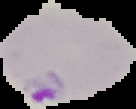

Summary:
  - Malaria status: parasitized
  - Image size: 136×109 pixels
  - Image type: cell region segmented out of the field of view; surrounding area masked to black
  - Preparation: thin blood smear